Assess the morphology of the erythrocytes.
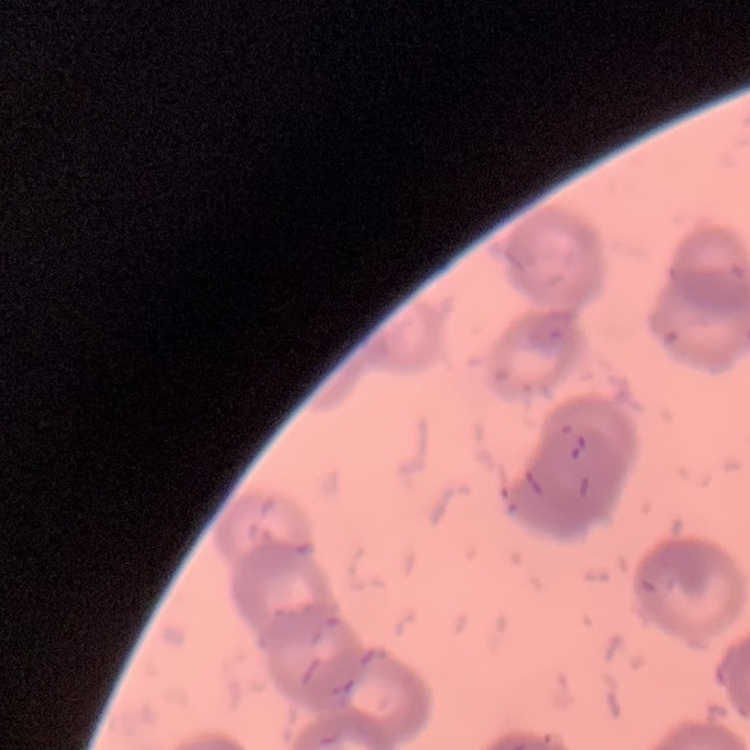
Rouleaux formation.

{
  "stain": "Field's or Giemsa",
  "image_type": "one tile cut from a larger photomicrograph",
  "preparation": "thin peripheral smear"
}